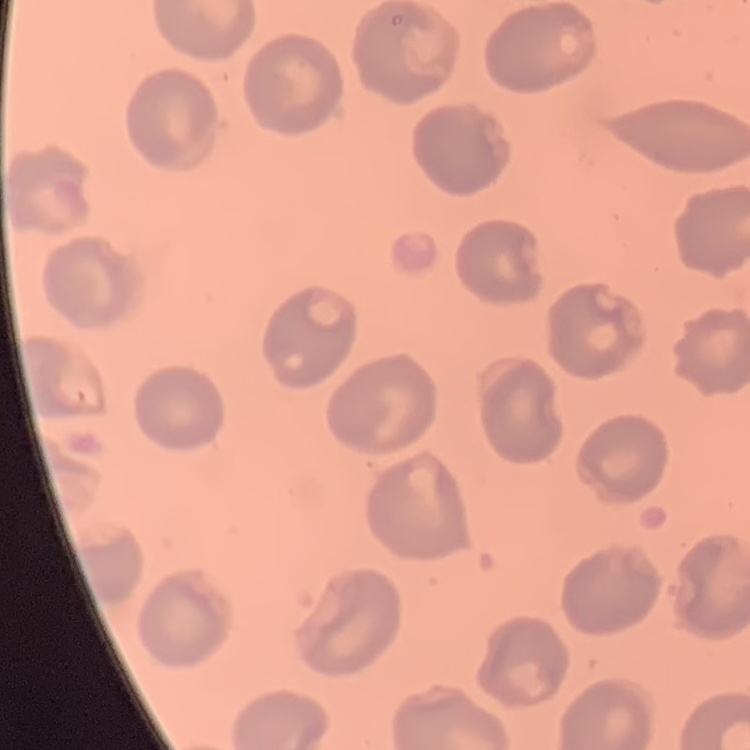
Summary:
  - Red blood cell morphology: no rouleaux formation
  - Image type: one tile cut from a larger photomicrograph
  - Stain: Field's or Giemsa
  - Preparation: thin blood film